Classify this cell by malaria status.
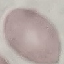

Uninfected.

Summary:
  - Capture: smartphone through the microscope eyepiece
  - Stain: Giemsa
  - Preparation: thin smear
  - Image type: cell patch, automatically extracted from a larger field of view and resized to 64 × 64 pixels